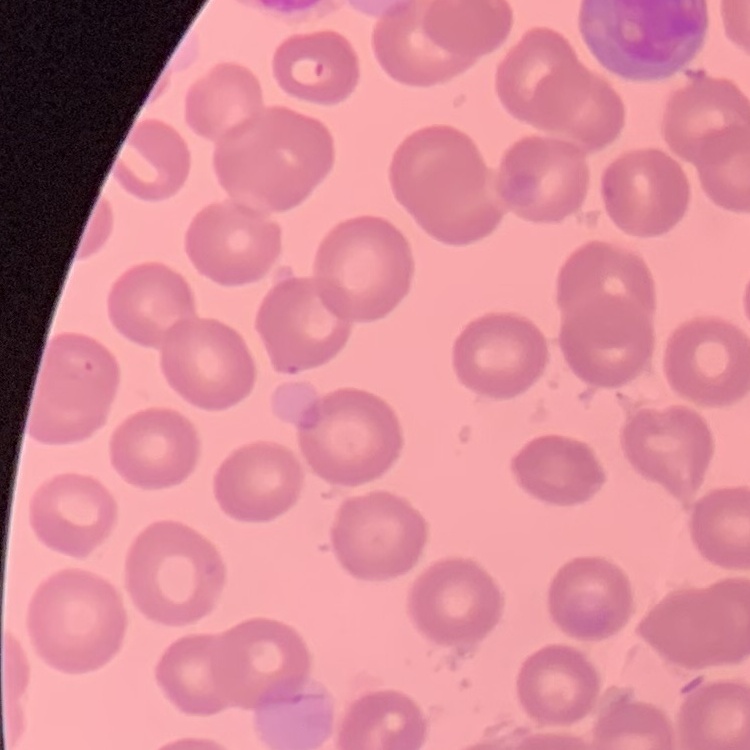

red_blood_cell_morphology: no rouleaux formation
image_type: one tile cut from a larger photomicrograph
preparation: thin blood film
stain: Field's or Giemsa